Assess this cell for malaria.
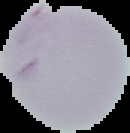

It is uninfected.

image type = segmented cell region on a black background
image size = 130×133 pixels
preparation = thin blood film